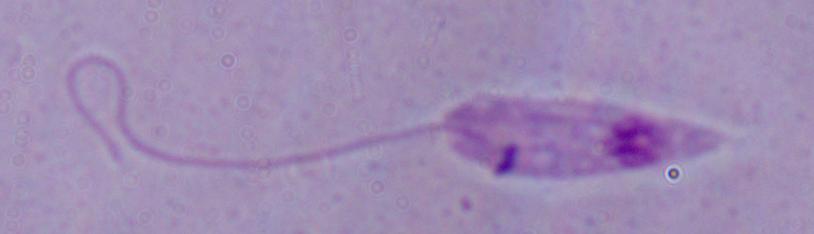
identification = Leishmania
modality = micrograph
magnification = 1000x